Locate every malaria parasite.
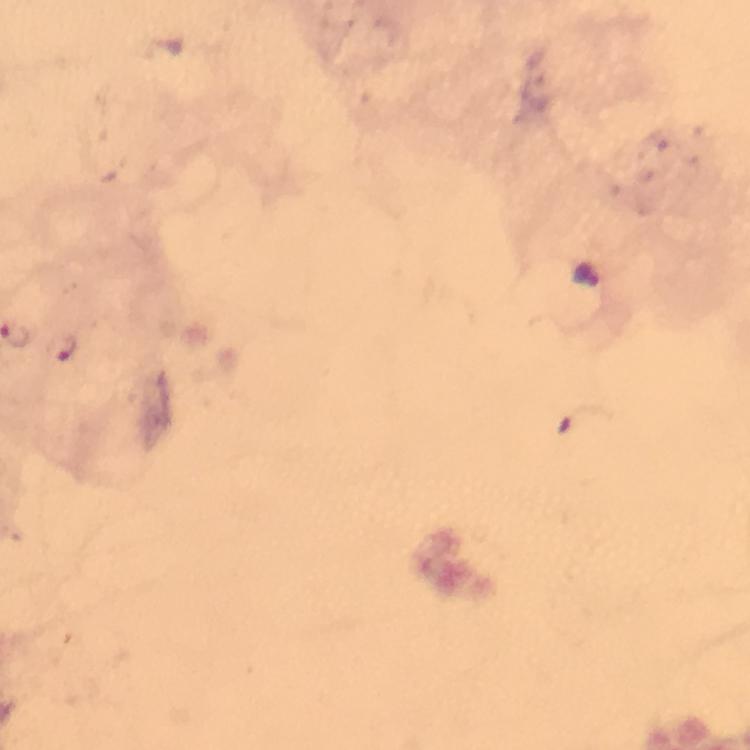
Approximate centers as {x, y} in pixels.
Malaria parasites: {69, 348}.

Summary:
  - Context: from a diagnostic examination for malaria
  - Capture: smartphone camera through the microscope
  - Stain: Giemsa
  - Preparation: thick blood smear
  - Cropped from: one field of view
  - Image size: 750×750 pixels
  - Magnification: 100x
  - Immersion oil: applied